Assess the morphology of the red blood cells.
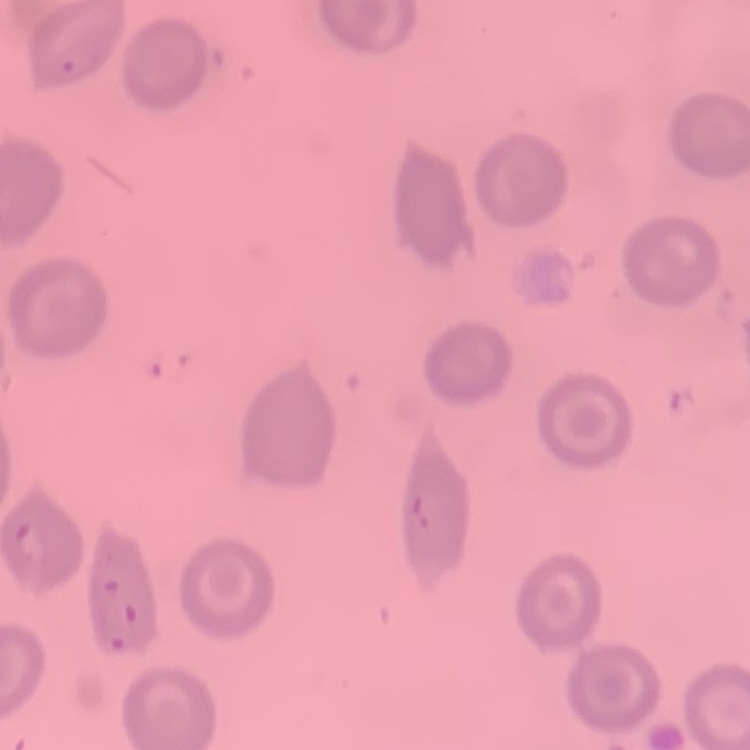

No rouleaux formation.

Square crop of a larger photomicrograph. Field's or Giemsa stain. Thin blood smear.